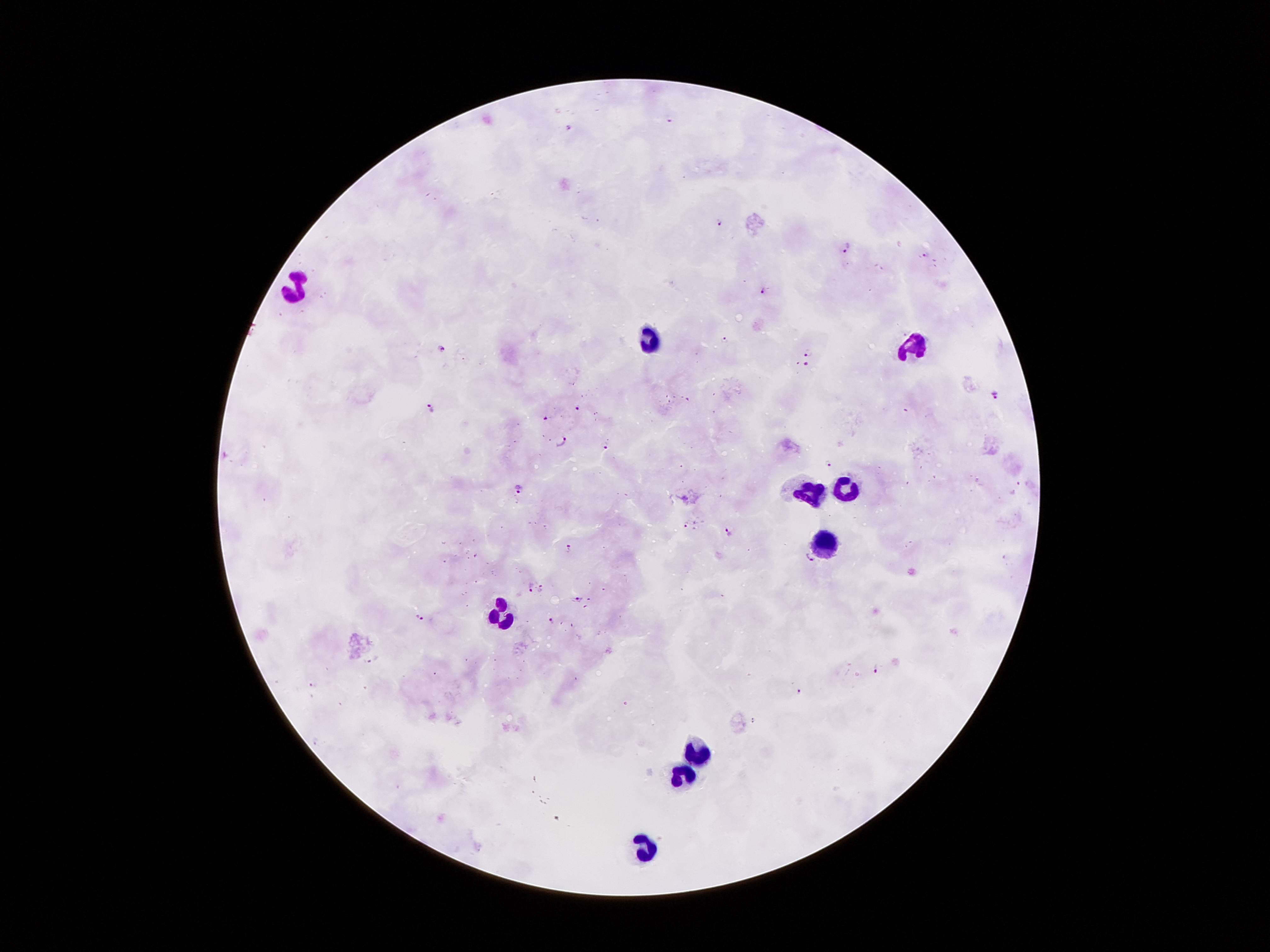
Approximate centers as (x, y) in pixels.
Summary:
  - Leukocyte locations: (295, 294), (651, 338), (912, 346), (843, 484), (804, 490), (821, 545), (499, 621), (699, 753), (682, 773), (643, 840)
  - Malaria parasite locations: (671, 117), (569, 128), (720, 222), (847, 248), (924, 254), (763, 290), (725, 341), (444, 347), (809, 352), (804, 363), (997, 393), (432, 408), (577, 408), (546, 416), (561, 444), (607, 448), (829, 463), (518, 489), (684, 523), (728, 533), (569, 550), (811, 560), (530, 587), (541, 587), (576, 599), (421, 617), (554, 622), (370, 660), (879, 667), (313, 684), (799, 691)
  - Field of view: single
  - Capture: smartphone camera through the microscope eyepiece
  - Patient malaria status: infected with Plasmodium falciparum
  - Stain: Giemsa
  - Magnification: 100x
  - Preparation: thick peripheral-blood smear
  - Image size: 1270×952 pixels